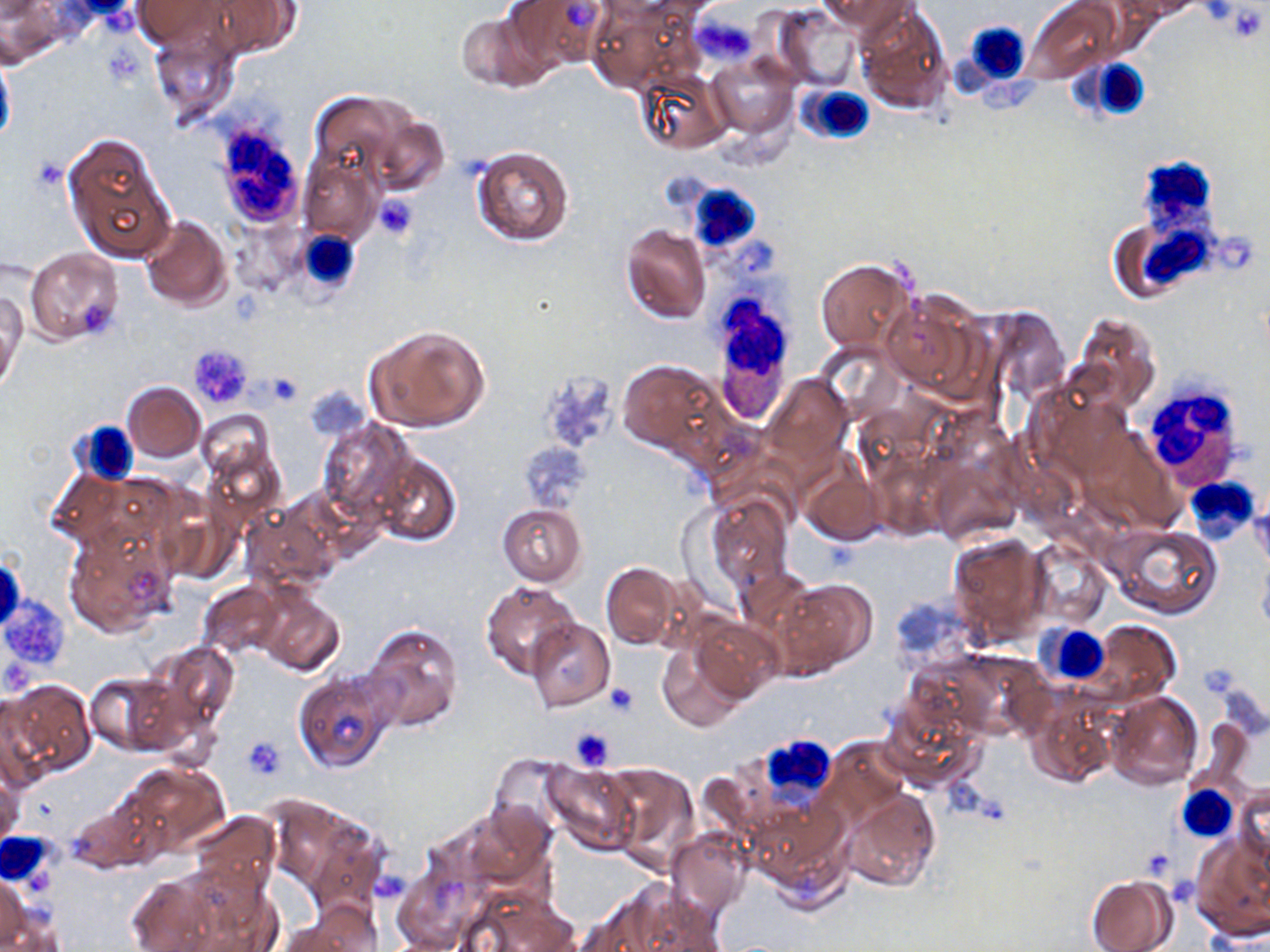

slide_level_diagnosis: negative for blood parasites
preparation: thin blood film
stain: May-Grünwald-Giemsa
field_of_view: one of a larger specimen
white_blood_cell_locations: 'approximate bounding boxes as (x1, y1, x2, y2) in pixels: (949, 21, 1034, 109), (1082, 57, 1152, 121), (796, 84, 877, 146), (209, 118, 308, 230), (1137, 154, 1226, 223), (667, 173, 772, 258), (1142, 224, 1244, 289), (293, 229, 365, 300), (708, 303, 794, 422), (1141, 375, 1248, 488), (72, 423, 137, 488), (1184, 475, 1259, 544), (1037, 623, 1109, 686), (755, 735, 837, 804), (1177, 785, 1236, 840), (2, 832, 55, 887)'
platelet_locations: 'approximate bounding boxes as (x1, y1, x2, y2) in pixels: (1222, 3, 1268, 43), (697, 17, 756, 65), (374, 195, 417, 240), (188, 343, 252, 409), (259, 372, 304, 404), (522, 439, 588, 511), (1, 595, 72, 674), (605, 681, 639, 717), (569, 727, 614, 770), (244, 736, 285, 778), (373, 872, 410, 906)'
image_size: 1270×952 pixels
magnification: 1000x
modality: optical microscopy
uninfected_red_blood_cell_locations: 'approximate bounding boxes as (x1, y1, x2, y2) in pixels: (132, 0, 229, 49), (504, 0, 610, 73), (820, 0, 912, 35), (1026, 0, 1119, 83), (1131, 0, 1201, 19), (201, 1, 305, 59), (855, 2, 953, 113), (587, 5, 689, 91), (775, 7, 862, 92), (454, 8, 548, 92), (148, 26, 240, 127), (0, 46, 16, 152), (706, 54, 798, 137), (636, 70, 730, 154), (309, 89, 412, 185), (366, 113, 450, 197), (63, 130, 176, 264), (470, 145, 574, 247), (299, 154, 381, 242), (140, 214, 232, 311), (618, 224, 710, 324), (24, 247, 124, 345), (815, 257, 915, 353), (824, 270, 949, 390), (880, 290, 988, 399), (1, 291, 25, 389), (980, 305, 1070, 404), (1070, 311, 1162, 414), (364, 325, 490, 433), (617, 360, 724, 457), (762, 373, 853, 472), (122, 381, 205, 461), (1028, 381, 1135, 484), (197, 409, 275, 486), (317, 418, 418, 524), (202, 440, 286, 531), (927, 450, 1021, 548), (370, 453, 460, 546), (799, 456, 887, 546), (45, 465, 131, 550), (1250, 487, 1270, 574), (704, 493, 794, 592), (157, 501, 242, 589), (241, 501, 341, 594), (497, 503, 587, 586), (63, 522, 179, 638), (1108, 523, 1224, 619), (948, 534, 1049, 647), (1028, 542, 1111, 627), (1258, 552, 1270, 637), (601, 563, 681, 650), (736, 566, 816, 641), (772, 578, 877, 678), (198, 579, 284, 659), (481, 580, 581, 680), (255, 588, 345, 677), (527, 618, 615, 710), (694, 619, 782, 701), (359, 621, 462, 733), (1088, 621, 1180, 706), (149, 640, 241, 734), (658, 645, 744, 732), (926, 649, 1047, 742), (85, 671, 179, 755), (292, 671, 395, 773), (4, 679, 95, 779), (1105, 691, 1202, 791), (1024, 692, 1118, 790), (0, 693, 52, 793), (878, 698, 982, 790), (1190, 719, 1254, 794), (821, 738, 910, 827), (489, 755, 572, 838), (125, 762, 229, 853), (542, 762, 637, 852), (602, 762, 696, 863), (0, 770, 23, 850), (1233, 784, 1269, 876), (840, 788, 941, 892), (66, 792, 160, 875), (753, 794, 853, 905), (456, 802, 558, 897), (188, 812, 280, 897), (304, 826, 386, 923), (664, 827, 751, 922), (1190, 837, 1270, 938), (169, 862, 280, 951), (125, 868, 231, 952), (1, 871, 31, 950), (1086, 876, 1175, 952), (589, 880, 724, 952), (462, 887, 578, 952), (284, 905, 380, 952)'